Name the cell type shown.
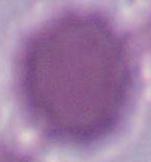

This is an erythrocyte.

1000x magnification. Micrograph.